Locate every blood parasite and identify its species.
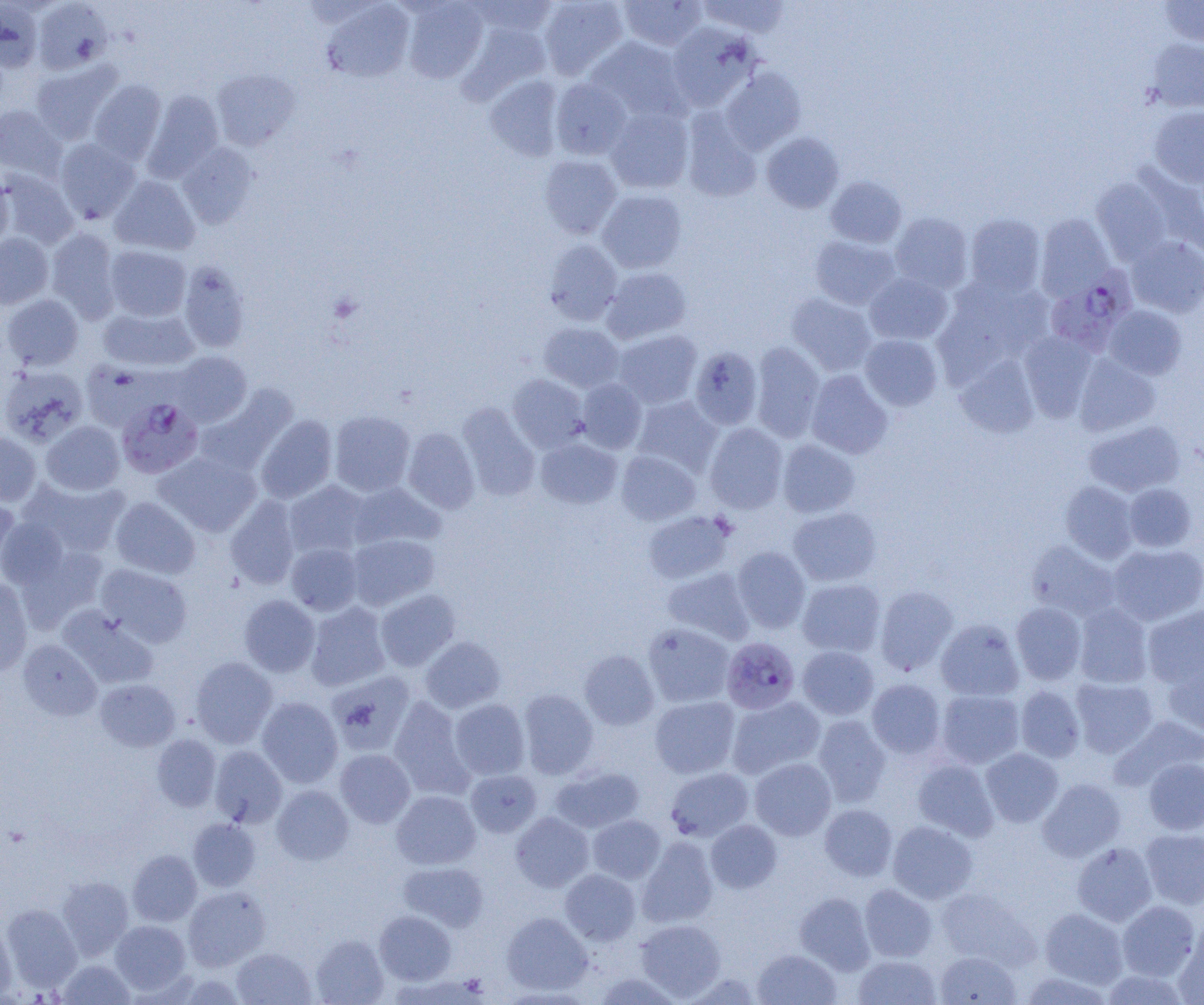
Approximate bounding boxes as (x1, y1, x2, y2) in pixels.
Plasmodium falciparum-infected red blood cells: (1045, 268, 1136, 353), (117, 397, 203, 478), (721, 637, 800, 714).
No Plasmodium ovale, Plasmodium malariae, Plasmodium vivax, Babesia divergens, or Trypanosoma brucei observed.

Uninfected red blood cell locations: (469, 0, 559, 38), (538, 0, 629, 80), (618, 0, 707, 51), (698, 0, 791, 38), (1158, 0, 1204, 47), (33, 1, 112, 74), (402, 1, 488, 83), (0, 2, 42, 73), (322, 2, 414, 83), (461, 21, 552, 100), (667, 22, 760, 110), (586, 37, 690, 124), (1146, 38, 1204, 112), (31, 61, 122, 143), (721, 67, 805, 154), (212, 69, 300, 151), (484, 75, 564, 161), (550, 78, 632, 160), (88, 79, 166, 164), (142, 90, 224, 182), (0, 105, 66, 181), (605, 106, 694, 194), (1148, 106, 1204, 188), (681, 110, 762, 203), (761, 132, 844, 213), (55, 138, 141, 224), (177, 142, 258, 228), (539, 154, 622, 239), (1136, 165, 1204, 257), (1, 169, 78, 248), (0, 173, 14, 251), (110, 175, 200, 256), (825, 176, 907, 247), (1091, 178, 1173, 264), (597, 189, 687, 273), (890, 213, 973, 294), (965, 213, 1046, 298), (1035, 213, 1114, 300), (46, 228, 121, 322), (0, 233, 53, 309), (810, 236, 900, 310), (1127, 236, 1204, 318), (543, 239, 623, 325), (104, 245, 191, 321), (178, 261, 250, 353), (602, 267, 691, 343), (864, 272, 953, 345), (933, 276, 1054, 379), (786, 293, 877, 376), (1, 294, 84, 370), (1103, 305, 1187, 380), (98, 306, 198, 372), (538, 323, 624, 392), (614, 329, 702, 409), (1019, 331, 1097, 422), (859, 334, 942, 412), (750, 342, 825, 442), (689, 346, 763, 430), (168, 351, 252, 427), (1074, 354, 1161, 437), (955, 355, 1040, 438), (80, 361, 164, 433), (0, 364, 88, 447), (805, 370, 893, 459), (508, 374, 589, 452), (577, 379, 646, 453), (195, 385, 297, 475), (632, 395, 722, 477), (457, 403, 540, 500), (330, 410, 415, 497), (255, 415, 338, 503), (1084, 419, 1185, 497), (41, 420, 125, 495), (705, 423, 788, 514), (403, 427, 480, 513), (0, 431, 41, 506), (536, 437, 622, 508), (777, 439, 860, 518), (155, 450, 261, 536), (616, 451, 701, 525), (20, 477, 129, 558), (284, 481, 370, 558), (1060, 481, 1138, 563), (348, 482, 446, 550), (1123, 483, 1197, 552), (0, 495, 21, 576), (110, 496, 200, 579), (225, 496, 301, 589), (788, 507, 881, 586), (643, 511, 734, 584), (0, 518, 69, 589), (346, 533, 440, 610), (1026, 540, 1120, 621), (286, 543, 363, 615), (1108, 543, 1204, 626), (16, 544, 108, 630), (732, 546, 811, 633), (95, 563, 192, 647), (662, 567, 755, 645), (797, 578, 885, 657), (0, 579, 32, 677), (874, 585, 958, 675), (376, 589, 461, 671), (239, 595, 320, 677), (305, 602, 391, 691), (1011, 602, 1087, 685), (1074, 604, 1153, 688), (58, 605, 158, 688), (1142, 605, 1204, 688), (936, 618, 1024, 701), (643, 623, 735, 707), (421, 636, 506, 713), (17, 639, 102, 720), (797, 645, 879, 720), (579, 650, 659, 730), (191, 657, 277, 747), (1163, 657, 1204, 738), (326, 670, 416, 756), (1071, 678, 1158, 757), (94, 679, 180, 751), (866, 679, 946, 759), (1015, 685, 1086, 763), (518, 689, 598, 779), (935, 689, 1024, 768), (727, 695, 825, 778), (649, 696, 740, 779), (257, 697, 343, 788), (389, 697, 474, 799), (449, 699, 530, 779), (812, 714, 891, 806), (1110, 715, 1204, 791), (152, 734, 221, 811), (210, 745, 287, 827), (980, 748, 1063, 827), (335, 749, 415, 827), (749, 757, 836, 840), (912, 758, 998, 840), (1144, 758, 1204, 835), (551, 766, 644, 833), (665, 767, 753, 841), (466, 770, 542, 837), (1038, 778, 1126, 862), (272, 785, 354, 865), (391, 790, 481, 869), (819, 804, 897, 881), (510, 812, 594, 892), (587, 815, 665, 884), (187, 818, 261, 892), (706, 820, 781, 893), (887, 821, 977, 904), (1140, 829, 1204, 909), (637, 836, 718, 928), (1072, 842, 1157, 926), (128, 850, 202, 926), (399, 861, 489, 932), (560, 869, 641, 945), (56, 876, 133, 959), (859, 883, 937, 962), (183, 886, 271, 970), (936, 888, 1039, 970), (795, 893, 875, 974), (1117, 901, 1200, 981), (2, 904, 81, 990), (1039, 908, 1128, 988), (374, 910, 456, 985), (502, 912, 592, 995), (635, 919, 726, 1000), (109, 920, 191, 995), (0, 921, 17, 1001), (1175, 925, 1204, 1005), (311, 934, 388, 1005), (232, 948, 316, 1005), (753, 948, 841, 1004), (934, 950, 1021, 1005), (853, 954, 941, 1004), (56, 958, 135, 1004), (1100, 969, 1191, 1005), (592, 972, 684, 1004), (681, 972, 761, 1004), (1017, 972, 1114, 1004). Slide-level diagnosis: Plasmodium falciparum. Thin blood smear. 1000x magnification. Single field of view. Image is 1204×1005 pixels. Light microscopy.